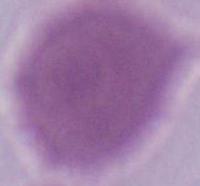
magnification = 1000x
identification = red blood cell
modality = photomicrograph